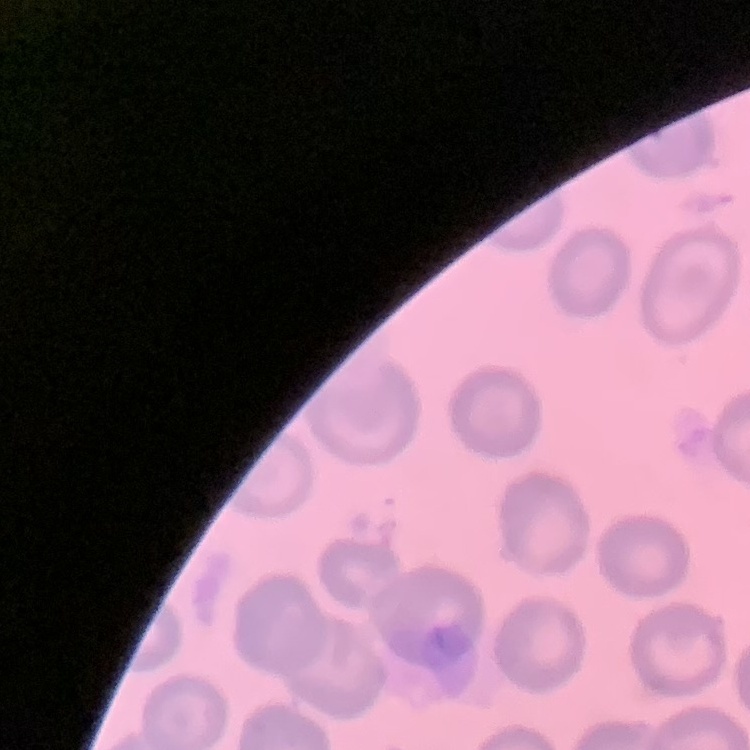
The erythrocytes exhibit no rouleaux formation. One tile cut from a larger photomicrograph. Stained with either Field's or Giemsa. Thin blood film.